Outline each uninfected red blood cell.
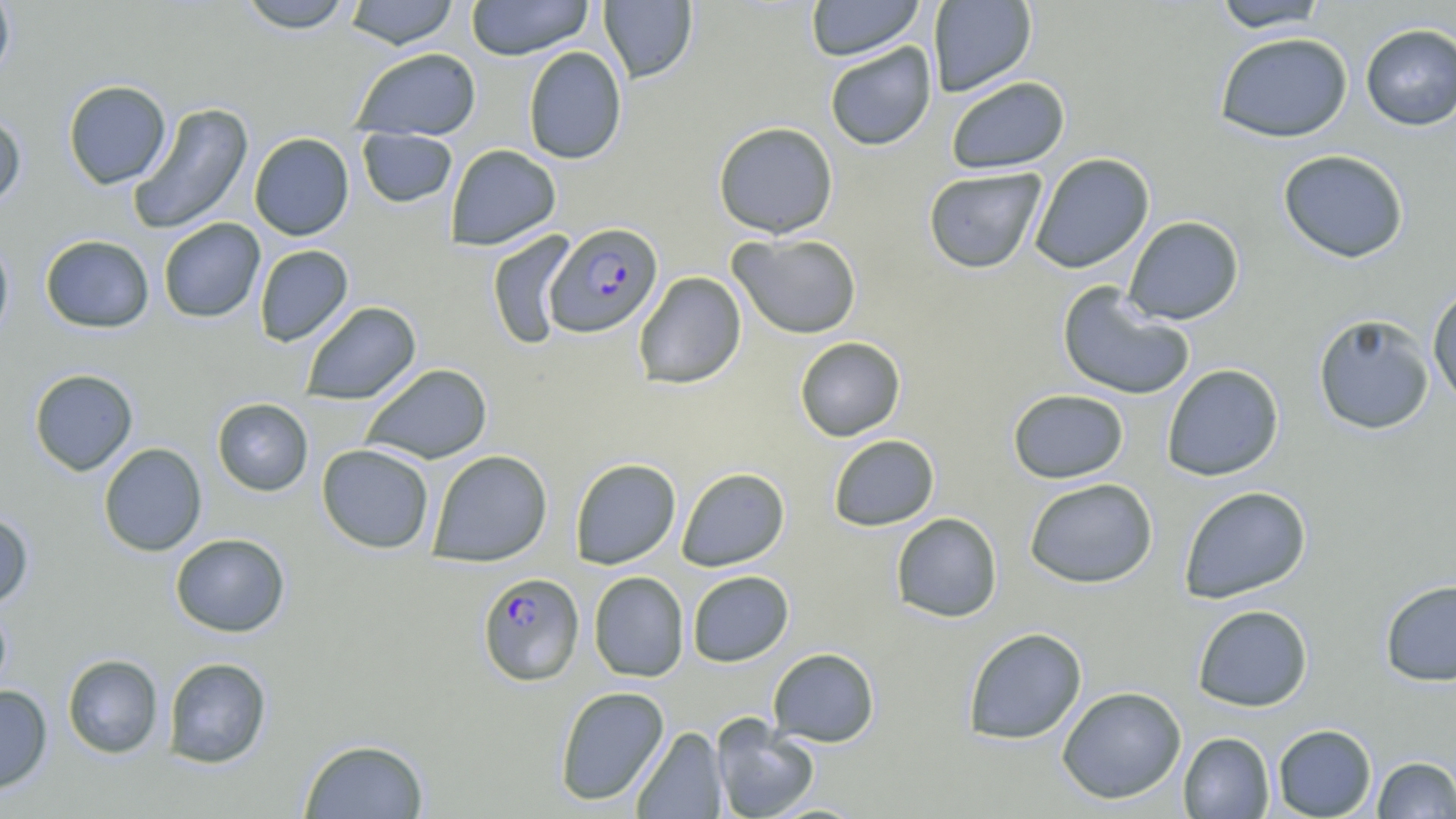

Approximate bounding boxes as (x1,y1)-(x2,y2) corner pairs in pixels.
Uninfected red blood cells: (0,0)-(16,84), (235,0)-(356,32), (342,0)-(459,49), (465,0)-(594,60), (805,0)-(925,61), (928,0)-(1037,97), (598,1)-(697,82), (1211,1)-(1331,33), (1360,23)-(1456,131), (1214,31)-(1353,143), (824,42)-(937,151), (523,46)-(627,164), (350,47)-(482,140), (945,76)-(1070,174), (62,80)-(171,189), (127,103)-(254,236), (0,111)-(26,211), (713,121)-(839,238), (357,129)-(457,207), (249,133)-(355,241), (446,144)-(561,250), (1278,149)-(1409,263), (1029,152)-(1154,274), (923,167)-(1047,274), (1123,216)-(1244,325), (158,217)-(265,323), (486,230)-(578,350), (729,233)-(862,339), (40,234)-(155,333), (0,236)-(14,345), (254,245)-(353,346), (633,271)-(746,389), (1057,282)-(1196,401), (1427,283)-(1456,409), (300,301)-(421,405), (1313,314)-(1435,435), (794,336)-(906,441), (360,363)-(492,464), (1161,363)-(1285,481), (29,368)-(138,475), (1007,389)-(1129,483), (212,398)-(314,496), (828,434)-(940,531), (98,443)-(207,556), (317,443)-(435,554), (428,450)-(553,567), (569,457)-(681,569), (676,467)-(790,571), (1024,477)-(1158,588), (1178,485)-(1311,604), (0,511)-(34,610), (890,512)-(1003,623), (170,533)-(290,637), (687,570)-(794,667), (588,571)-(689,682), (1379,579)-(1456,687), (0,601)-(13,705), (1192,604)-(1313,712), (962,627)-(1087,745), (767,647)-(880,747), (62,653)-(164,759), (162,657)-(272,769), (0,685)-(53,794), (554,685)-(670,806), (1056,686)-(1187,804), (711,716)-(820,819), (1272,723)-(1377,818), (631,726)-(727,818), (1178,731)-(1275,818), (298,738)-(430,818), (1372,756)-(1456,818).

slide-level diagnosis = Plasmodium falciparum
image size = 1456×819 pixels
Plasmodium falciparum-infected red blood cell locations = approximate bounding boxes as (x1,y1)-(x2,y2) corner pairs in pixels: (545,222)-(663,337), (477,572)-(584,686)
preparation = thin blood smear
magnification = 1000x
stain = May-Grünwald-Giemsa
field of view = one of a larger specimen
modality = light microscopy